Locate and identify every blood parasite.
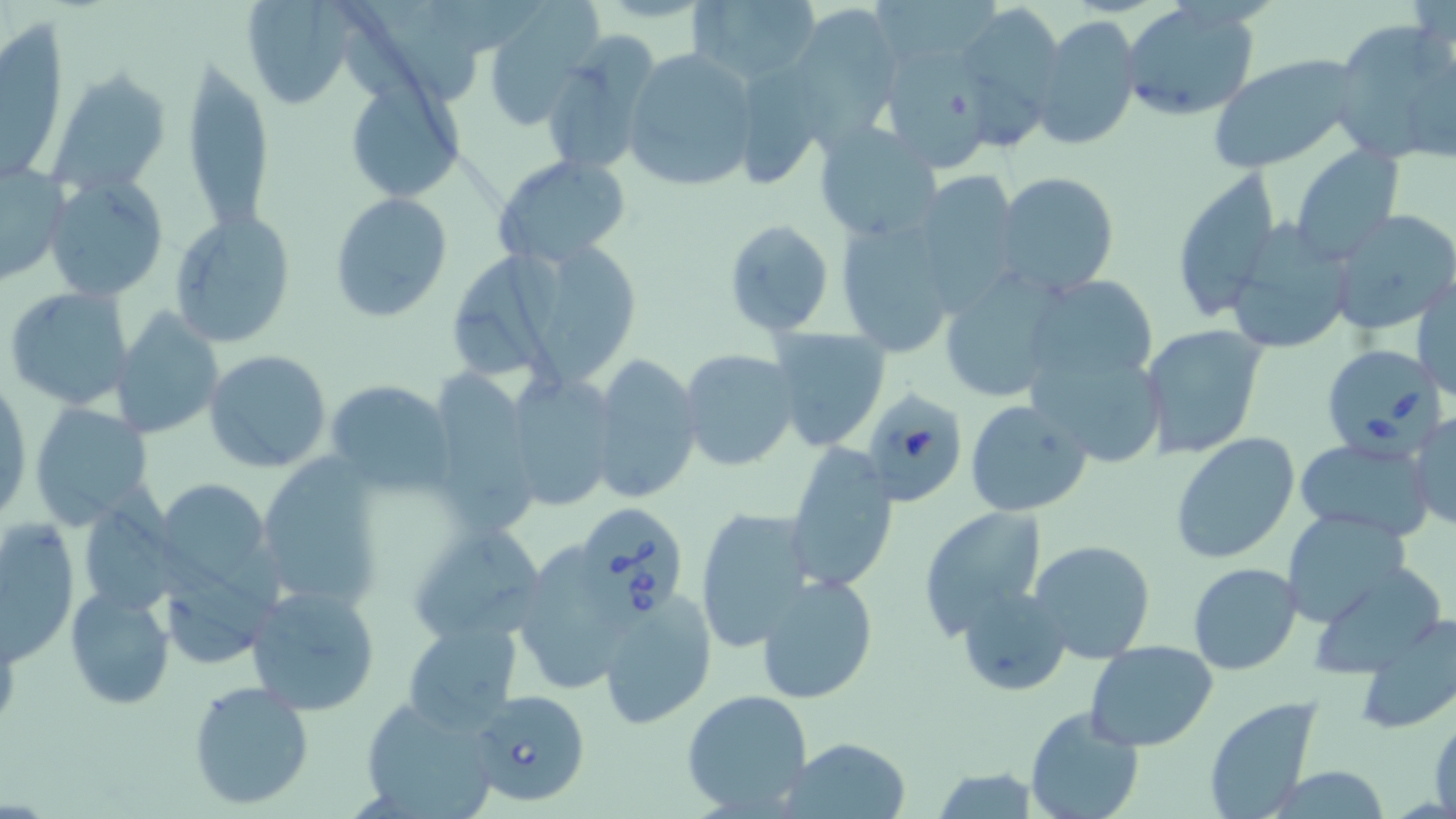

Approximate bounding boxes as (x1,y1)-(x2,y2) corner pairs in pixels.
Babesia divergens-infected red blood cells: (1320,343)-(1445,459), (860,385)-(970,508), (575,502)-(690,619), (469,688)-(592,807).
No Plasmodium falciparum, Plasmodium ovale, Plasmodium malariae, Plasmodium vivax, or Trypanosoma brucei observed.

{
  "slide_level_diagnosis": "Babesia divergens",
  "uninfected_red_blood_cell_locations": "approximate bounding boxes as (x1,y1)-(x2,y2) corner pairs in pixels: (239,0)-(356,110), (684,0)-(821,87), (1120,2)-(1259,122), (951,3)-(1064,131), (480,6)-(597,133), (786,6)-(902,145), (1030,14)-(1143,152), (2,17)-(67,185), (1330,21)-(1456,166), (535,37)-(659,178), (623,46)-(760,193), (879,50)-(996,175), (1208,54)-(1362,174), (183,58)-(273,235), (49,69)-(168,194), (342,75)-(467,202), (812,121)-(944,242), (1289,146)-(1404,264), (490,153)-(630,266), (0,163)-(69,286), (1170,168)-(1282,320), (993,171)-(1121,299), (44,174)-(167,301), (913,174)-(1023,312), (329,193)-(452,321), (1329,208)-(1456,337), (168,211)-(299,348), (833,215)-(962,360), (722,218)-(835,339), (1225,222)-(1353,356), (530,240)-(634,386), (455,248)-(577,381), (937,267)-(1070,405), (1020,275)-(1160,389), (1414,276)-(1454,403), (5,285)-(134,410), (113,309)-(224,441), (1137,322)-(1267,459), (768,327)-(890,452), (1026,342)-(1169,470), (204,348)-(333,473), (678,348)-(800,471), (587,355)-(701,505), (425,371)-(541,533), (503,373)-(620,512), (0,377)-(30,525), (324,379)-(454,495), (963,398)-(1094,519), (30,399)-(155,527), (1409,412)-(1454,531), (1169,432)-(1300,565), (1296,439)-(1434,541), (784,442)-(899,594), (256,452)-(388,614), (158,479)-(272,594), (77,496)-(181,618), (693,505)-(813,653), (918,506)-(1049,638), (1279,510)-(1411,629), (1,517)-(82,666), (406,521)-(548,646), (1028,539)-(1156,666), (510,544)-(642,697), (1188,562)-(1302,675), (1304,564)-(1448,678), (756,572)-(878,705), (245,583)-(381,716), (64,585)-(175,710), (955,586)-(1070,698), (596,591)-(717,729), (1356,612)-(1456,733), (403,622)-(523,736), (1085,640)-(1218,751), (187,680)-(314,811), (681,688)-(814,816), (357,695)-(503,819), (1202,697)-(1324,819), (1024,706)-(1145,819), (1430,710)-(1456,815), (785,736)-(912,817), (931,766)-(1041,819), (1261,766)-(1397,819)",
  "stain": "May-Grünwald-Giemsa",
  "preparation": "thin blood film",
  "modality": "optical microscopy",
  "field_of_view": "single",
  "image_size": "1456×819 pixels",
  "magnification": "1000x"
}